Identify the parasite.
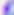
This is Toxoplasma gondii.

Summary:
  - Magnification: 400x
  - Modality: photomicrograph